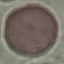
Result: no malaria parasites detected. Thin blood film. Giemsa stain. Cell patch, automatically extracted from a larger field of view and resized to 64 × 64 pixels. Photographed with a smartphone camera at the microscope eyepiece.